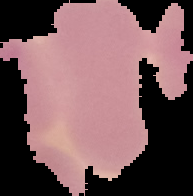
Summary:
  - Malaria status: uninfected
  - Image size: 193×196 pixels
  - Image type: segmented cell region with the area outside set to black
  - Preparation: thin blood film